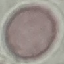
Summary:
  - Malaria status: uninfected
  - Preparation: thin blood film
  - Capture: smartphone through the microscope eyepiece
  - Stain: Giemsa
  - Image type: cell patch, automatically extracted from a larger field of view and resized to 64 × 64 pixels